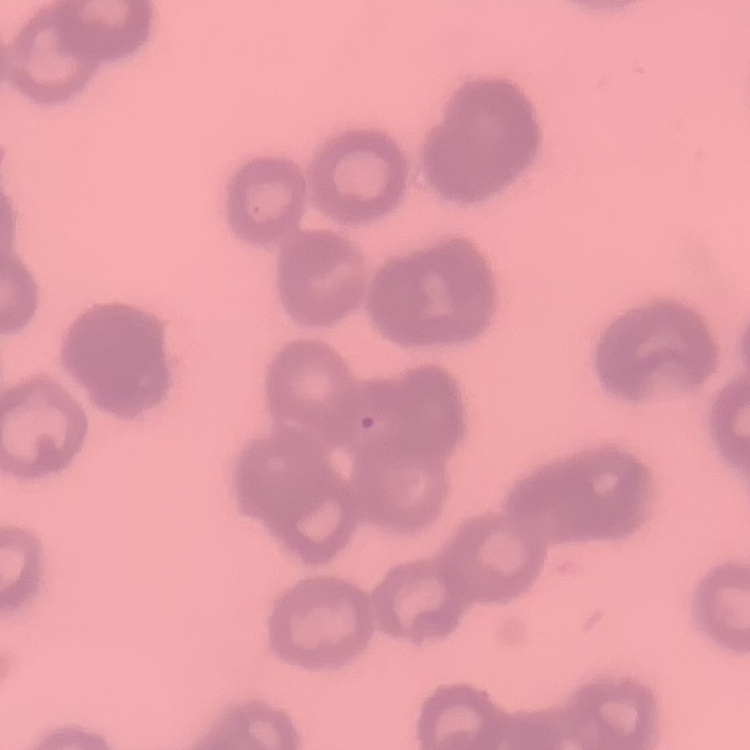

{
  "red_blood_cell_morphology": "rouleaux formation",
  "stain": "Field's or Giemsa",
  "image_type": "one tile cut from a larger photomicrograph",
  "preparation": "thin peripheral smear"
}